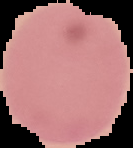
image size = 133×148 pixels
malaria status = uninfected
image type = cell region segmented out of the field of view; surrounding area masked to black
preparation = thin blood film